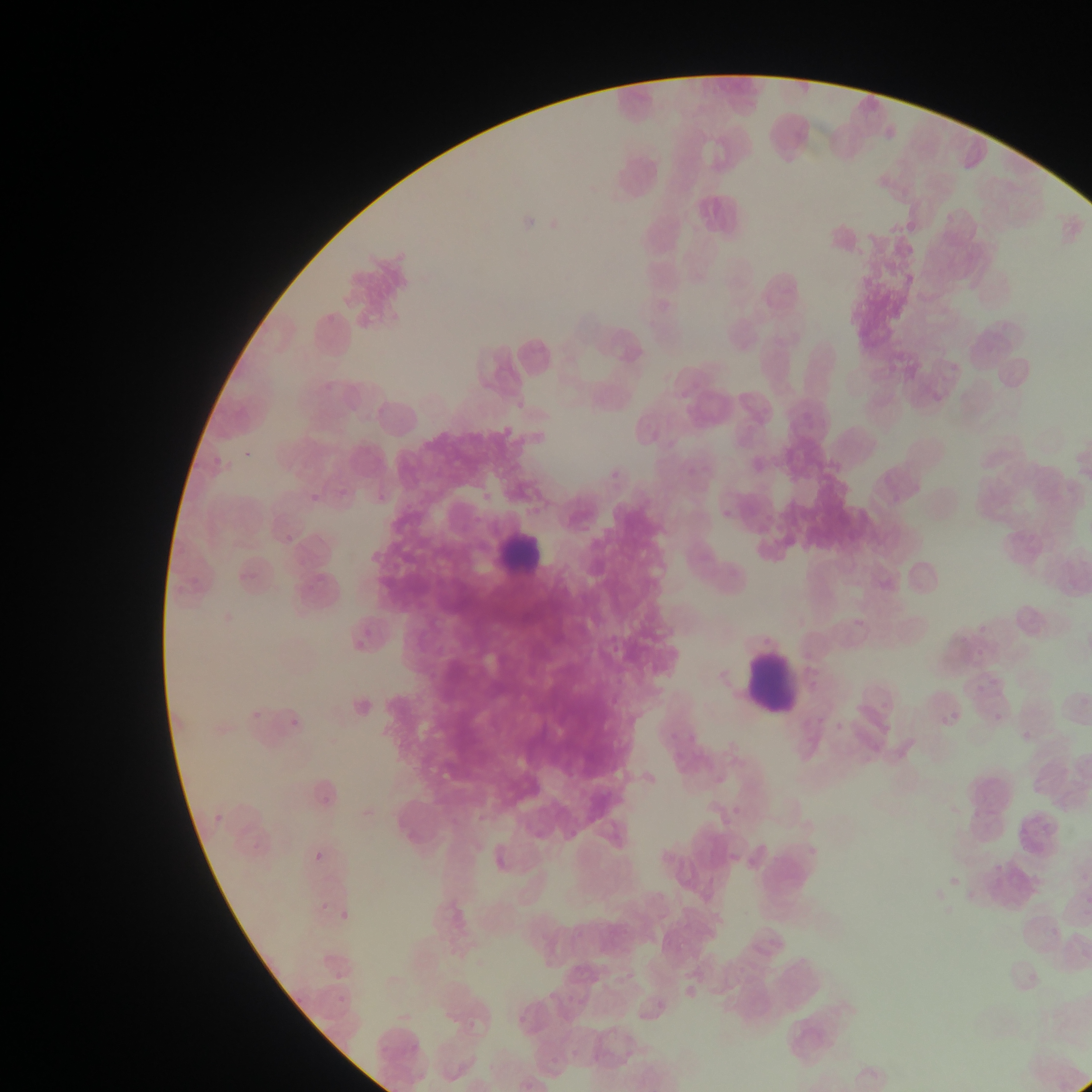 Approximate bounding boxes as [left, top, right, bottom] in pixels. Leukocyte locations: [494, 519, 552, 582], [746, 651, 800, 708]. Plasmodium parasite locations: [247, 447, 261, 454], [213, 454, 225, 477], [286, 534, 298, 544], [968, 641, 985, 661], [976, 677, 998, 699], [250, 705, 261, 721], [986, 706, 1006, 720], [930, 707, 963, 729], [288, 719, 300, 728], [213, 808, 233, 823], [314, 844, 330, 858], [950, 871, 967, 886], [318, 902, 327, 914], [336, 907, 355, 919]. Thin blood smear. Image is 1092×1092 pixels. Mobile-phone photograph taken through the microscope. Sample from Ghana. Single field of view.